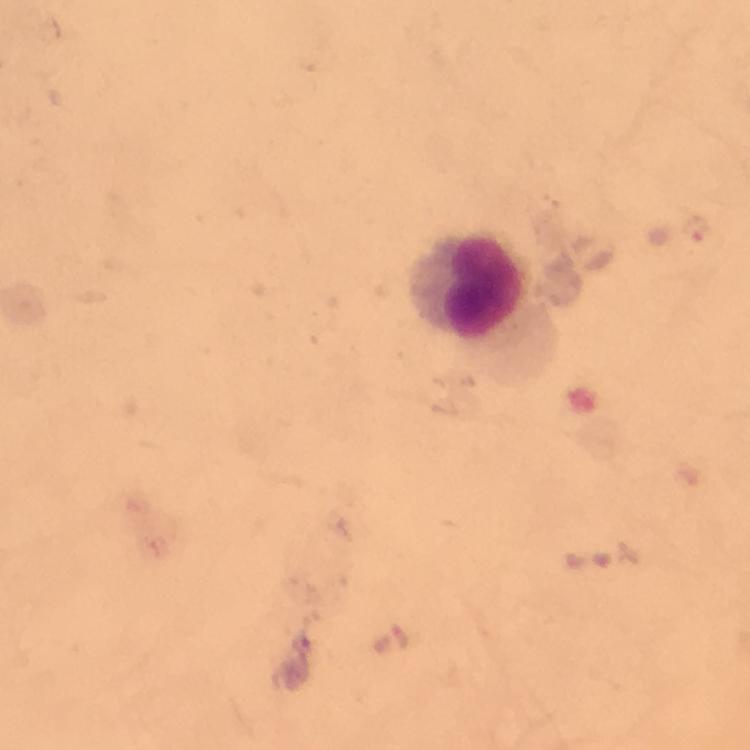

Approximate centers as (x, y) in pixels. Plasmodium parasite locations: (696, 228). Leukocyte locations: (464, 286). Image is 750×750 pixels. From a diagnostic examination for malaria. Smartphone photograph taken through a microscope. Immersion oil applied. Giemsa-stained preparation. A crop from one field of view. Thick blood smear. At 100x magnification.